Identify the parasite.
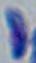
Toxoplasma gondii.

Summary:
  - Modality: photomicrograph
  - Magnification: 1000x